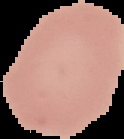
Summary:
  - Preparation: thin blood smear
  - Result: no malaria parasites seen
  - Image size: 124×139 pixels
  - Image type: segmented cell region on a black background